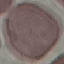 Malaria status: uninfected. Cell patch, automatically extracted from a larger field of view and resized to 64 × 64 pixels. Giemsa stain. Photographed with a smartphone camera at the microscope eyepiece. Thin blood film.